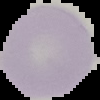
{
  "image_size": "100×100 pixels",
  "malaria_status": "uninfected",
  "image_type": "segmented cell region with the area outside set to black",
  "preparation": "thin blood film"
}